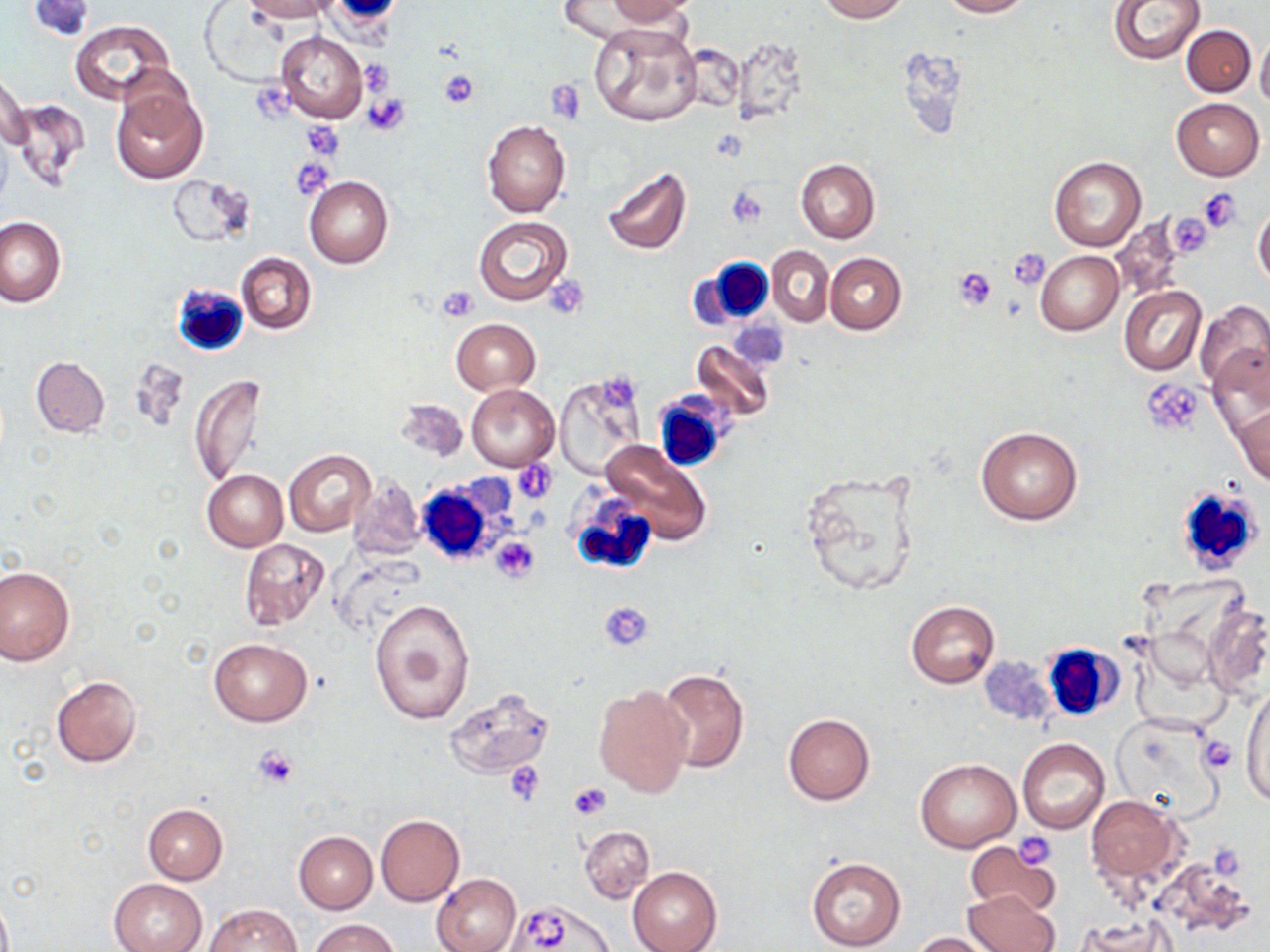

Summary:
  - Coordinate format: approximate bounding boxes as (x1,y1)-(x2,y2) corner pairs in pixels
  - Uninfected red blood cell locations: (242,0)-(332,21), (595,0)-(699,26), (817,0)-(906,21), (940,0)-(1030,17), (1108,0)-(1206,63), (202,4)-(286,84), (70,21)-(174,106), (590,22)-(701,128), (1182,24)-(1255,96), (274,30)-(367,122), (1256,31)-(1270,112), (678,41)-(745,114), (0,69)-(31,155), (109,86)-(207,185), (1171,98)-(1264,179), (9,99)-(88,188), (292,120)-(353,161), (483,120)-(571,218), (1048,155)-(1147,252), (795,159)-(879,243), (602,167)-(690,257), (167,173)-(251,249), (303,176)-(395,267), (1253,206)-(1270,288), (1110,214)-(1191,301), (473,215)-(572,306), (0,216)-(68,307), (768,246)-(833,327), (1035,249)-(1123,335), (235,252)-(317,334), (825,252)-(906,334), (1118,285)-(1205,376), (1195,301)-(1270,392), (452,319)-(540,394), (692,340)-(776,421), (1207,344)-(1270,436), (30,356)-(109,437), (191,375)-(269,486), (554,378)-(643,477), (465,384)-(559,471), (396,398)-(467,462), (1231,403)-(1270,487), (975,427)-(1082,523), (599,440)-(712,546), (283,449)-(373,537), (799,466)-(927,599), (202,469)-(288,552), (348,474)-(425,560), (239,537)-(330,630), (0,565)-(74,667), (368,598)-(475,725), (907,600)-(999,689), (1203,603)-(1270,699), (207,638)-(312,727), (980,654)-(1058,726), (656,669)-(750,774), (51,675)-(143,768), (593,684)-(692,798), (1241,687)-(1268,809), (443,688)-(555,779), (783,713)-(875,804), (1108,714)-(1222,818), (1017,739)-(1110,834), (915,758)-(1021,853), (1085,794)-(1181,884), (142,804)-(228,884), (375,814)-(464,907), (579,825)-(655,904), (294,831)-(377,912), (966,843)-(1055,919), (807,857)-(905,950), (627,866)-(721,952), (432,873)-(522,952), (107,877)-(207,952), (963,891)-(1060,952), (0,894)-(13,952), (507,899)-(613,951), (203,903)-(300,952), (1078,915)-(1173,952), (309,919)-(399,952), (914,932)-(999,952)
  - White blood cell locations: (695,255)-(780,329), (171,284)-(256,357), (650,393)-(729,470), (412,478)-(504,567), (1174,486)-(1266,578), (570,493)-(659,576), (1040,643)-(1121,722)
  - Platelet locations: (32,0)-(96,42), (358,61)-(392,96), (437,70)-(480,109), (545,82)-(587,121), (253,86)-(299,122), (363,95)-(409,134), (302,122)-(345,158), (728,187)-(768,226), (1198,189)-(1243,232), (1178,213)-(1216,258), (1007,247)-(1050,289), (953,269)-(998,310), (544,277)-(590,318), (436,286)-(480,322), (601,370)-(639,408), (1143,380)-(1206,436), (515,461)-(557,503), (490,537)-(540,583), (600,601)-(654,650), (1199,734)-(1237,776), (253,746)-(299,789), (505,761)-(546,805), (567,782)-(613,820), (1016,831)-(1058,868), (523,911)-(574,947)
  - Slide-level diagnosis: negative for blood parasites
  - Modality: optical microscopy
  - Stain: May-Grünwald-Giemsa
  - Magnification: 1000x
  - Image size: 1270×952 pixels
  - Field of view: single
  - Preparation: thin blood smear